Identify the blood parasite species.
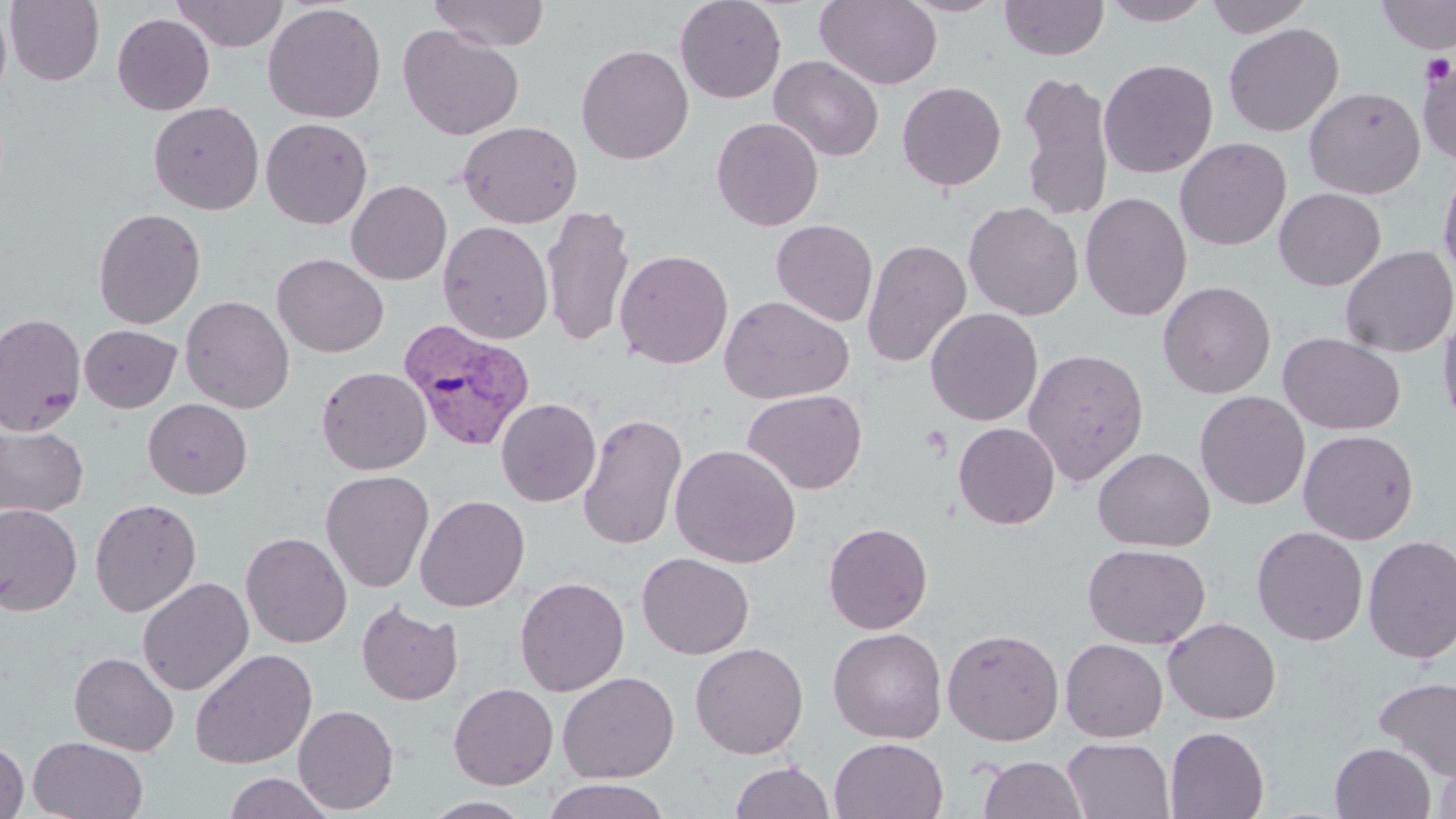
Plasmodium vivax.

Approximate bounding boxes as (x1,y1)-(x2,y2) corner pairs in pixels. Plasmodium vivax-infected red blood cell locations: (399,318)-(536,453). Uninfected red blood cell locations: (4,0)-(105,86), (171,0)-(289,51), (428,0)-(550,51), (675,0)-(786,103), (815,0)-(942,89), (897,0)-(1010,17), (999,0)-(1109,61), (1100,0)-(1215,26), (1204,0)-(1314,37), (1376,0)-(1456,54), (263,3)-(386,123), (0,4)-(12,103), (111,13)-(215,115), (1224,23)-(1344,137), (398,25)-(524,140), (575,43)-(694,164), (769,55)-(884,161), (1417,55)-(1456,165), (1098,58)-(1218,179), (1017,70)-(1115,222), (896,81)-(1007,191), (1304,85)-(1425,199), (149,101)-(265,215), (711,116)-(824,230), (261,117)-(373,229), (457,120)-(583,228), (1175,137)-(1292,251), (1438,161)-(1456,287), (346,180)-(451,285), (1274,187)-(1386,291), (1079,192)-(1192,322), (963,201)-(1084,321), (541,204)-(636,348), (93,207)-(206,329), (771,219)-(878,327), (438,220)-(553,344), (861,238)-(971,368), (1340,245)-(1456,357), (614,248)-(733,369), (272,253)-(389,358), (1157,280)-(1276,398), (180,295)-(295,413), (719,295)-(853,404), (1437,304)-(1456,432), (925,307)-(1043,426), (0,312)-(86,437), (79,324)-(181,413), (1278,332)-(1406,435), (1023,347)-(1149,486), (316,366)-(431,474), (743,389)-(867,494), (1195,390)-(1310,509), (496,397)-(601,506), (143,398)-(252,499), (578,412)-(687,551), (953,422)-(1060,529), (0,424)-(90,519), (1299,429)-(1419,545), (670,444)-(801,568), (1093,447)-(1215,551), (320,469)-(434,592), (414,494)-(530,612), (90,497)-(203,617), (0,503)-(82,616), (823,521)-(933,634), (1251,525)-(1368,645), (240,531)-(352,648), (1363,534)-(1456,664), (1082,543)-(1210,649), (637,552)-(755,659), (515,576)-(630,696), (137,577)-(254,696), (356,600)-(464,706), (1163,617)-(1281,724), (828,627)-(947,743), (942,628)-(1064,746), (1060,638)-(1168,742), (689,642)-(809,759), (189,648)-(317,769), (70,652)-(179,756), (557,671)-(680,783), (1373,676)-(1456,781), (448,682)-(559,789), (293,704)-(400,814), (1165,726)-(1270,818), (28,736)-(149,819), (0,737)-(29,819), (830,737)-(949,819), (1062,737)-(1174,819), (1330,742)-(1436,819), (1434,752)-(1456,819), (978,754)-(1089,819), (730,760)-(835,819), (223,772)-(335,818), (541,778)-(672,818), (421,796)-(537,818). Platelet locations: (1420,53)-(1455,86), (921,425)-(953,461). Thin blood smear. Single field of view. May-Grünwald-Giemsa-stained preparation. 1000x magnification. Light microscopy. Image is 1456×819 pixels.